Describe the morphology of the red blood cells.
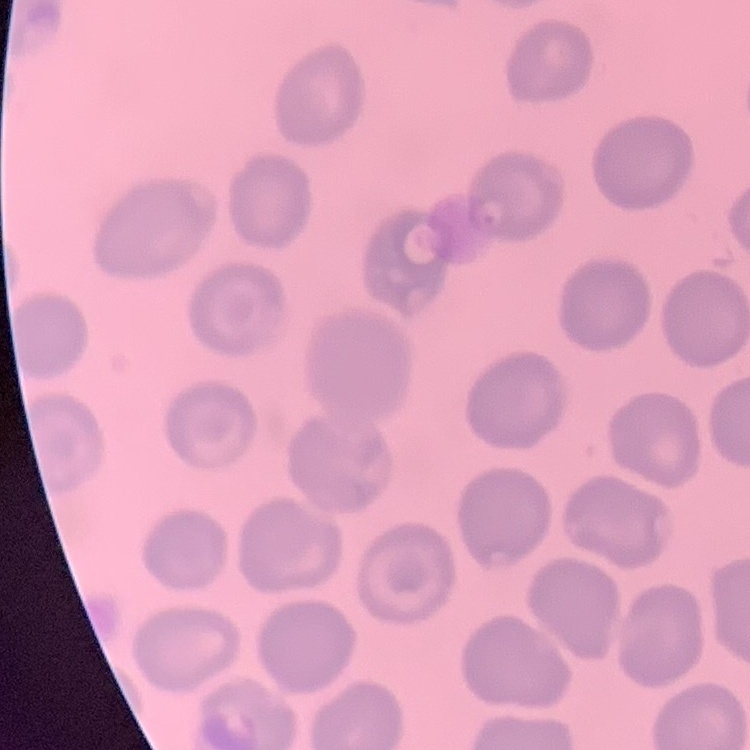
No rouleaux formation.

Stained with either Field's or Giemsa. Thin blood smear. Square crop of a larger photomicrograph.